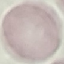
Malaria status: uninfected. Photographed with a smartphone camera at the microscope eyepiece. Thin blood film. Cell patch, automatically extracted from a larger field of view and resized to 64 × 64 pixels. Giemsa-stained preparation.